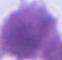

magnification = 1000x
modality = photomicrograph
identification = red blood cell